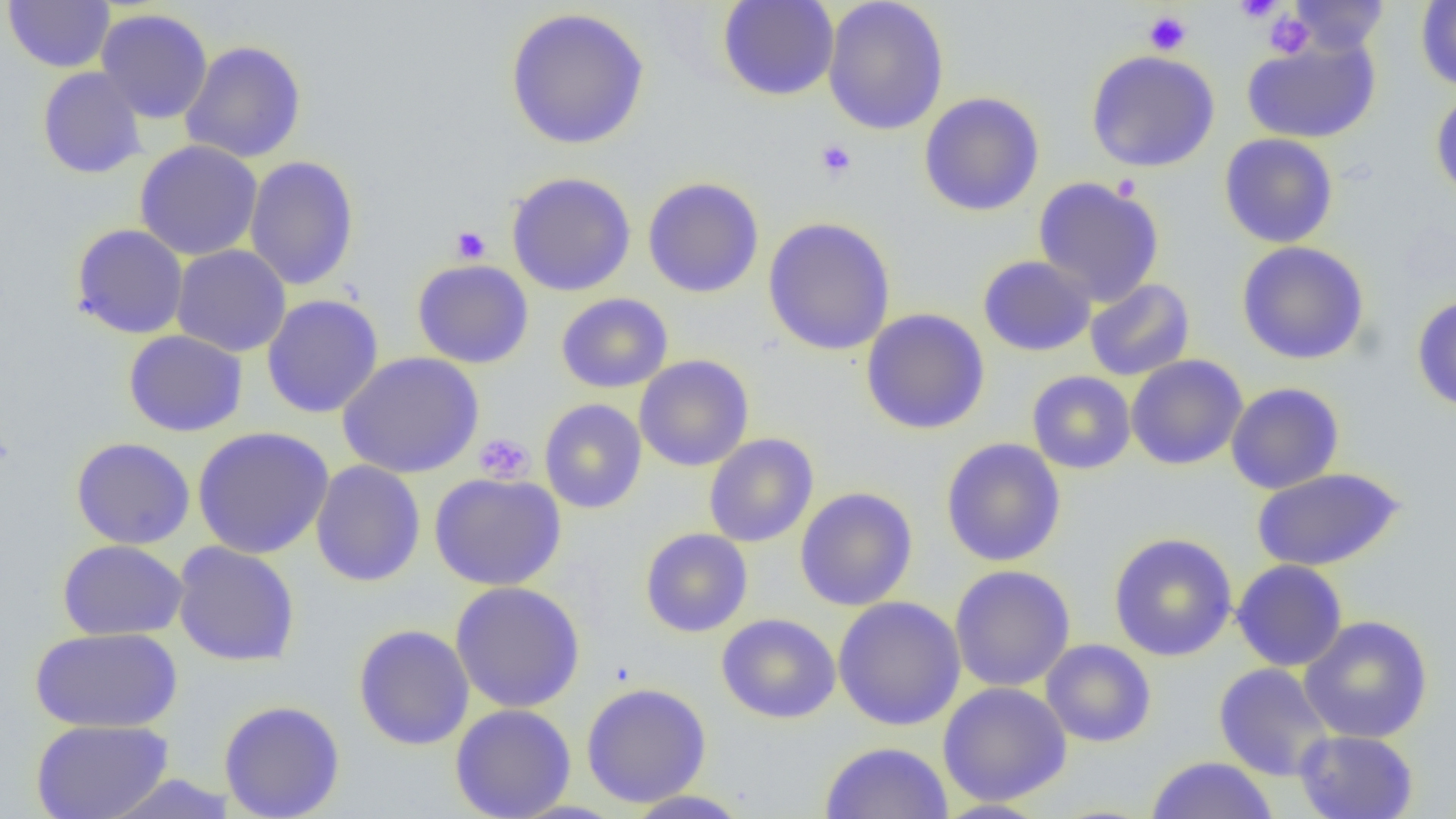

slide-level diagnosis = no evidence of blood parasites
image size = 1456×819 pixels
platelet locations = approximate bounding boxes as named x1/y1/x2/y2 corners in pixels: (x1=1234, y1=0, x2=1284, y2=23), (x1=1143, y1=11, x2=1192, y2=55), (x1=1264, y1=12, x2=1314, y2=59), (x1=815, y1=139, x2=857, y2=181), (x1=450, y1=226, x2=491, y2=264), (x1=474, y1=433, x2=536, y2=484)
magnification = 1000x
modality = optical microscopy
field of view = single
uninfected red blood cell locations = approximate bounding boxes as named x1/y1/x2/y2 corners in pixels: (x1=4, y1=0, x2=115, y2=73), (x1=717, y1=0, x2=840, y2=101), (x1=1288, y1=0, x2=1389, y2=54), (x1=822, y1=1, x2=950, y2=136), (x1=1416, y1=1, x2=1456, y2=91), (x1=505, y1=7, x2=650, y2=150), (x1=96, y1=8, x2=213, y2=124), (x1=1241, y1=36, x2=1380, y2=144), (x1=179, y1=40, x2=308, y2=163), (x1=1085, y1=49, x2=1220, y2=173), (x1=37, y1=67, x2=147, y2=179), (x1=1430, y1=89, x2=1456, y2=202), (x1=919, y1=91, x2=1045, y2=216), (x1=1218, y1=133, x2=1339, y2=248), (x1=134, y1=141, x2=263, y2=261), (x1=244, y1=155, x2=360, y2=290), (x1=507, y1=172, x2=636, y2=296), (x1=1033, y1=176, x2=1165, y2=307), (x1=642, y1=177, x2=765, y2=298), (x1=762, y1=216, x2=896, y2=356), (x1=71, y1=223, x2=188, y2=339), (x1=1236, y1=241, x2=1370, y2=365), (x1=171, y1=244, x2=291, y2=357), (x1=977, y1=255, x2=1096, y2=356), (x1=412, y1=259, x2=534, y2=369), (x1=1084, y1=278, x2=1195, y2=381), (x1=556, y1=292, x2=673, y2=393), (x1=261, y1=294, x2=384, y2=418), (x1=1411, y1=295, x2=1456, y2=413), (x1=860, y1=308, x2=990, y2=435), (x1=123, y1=330, x2=248, y2=437), (x1=337, y1=352, x2=484, y2=479), (x1=634, y1=355, x2=754, y2=472), (x1=1125, y1=355, x2=1248, y2=470), (x1=1026, y1=370, x2=1136, y2=474), (x1=1225, y1=382, x2=1345, y2=494), (x1=539, y1=398, x2=647, y2=514), (x1=192, y1=426, x2=334, y2=559), (x1=704, y1=432, x2=819, y2=547), (x1=70, y1=437, x2=195, y2=549), (x1=940, y1=438, x2=1066, y2=567), (x1=310, y1=460, x2=426, y2=587), (x1=1251, y1=467, x2=1405, y2=571), (x1=429, y1=472, x2=566, y2=591), (x1=794, y1=487, x2=918, y2=611), (x1=640, y1=528, x2=753, y2=637), (x1=1108, y1=532, x2=1238, y2=661), (x1=58, y1=539, x2=188, y2=641), (x1=172, y1=541, x2=300, y2=667), (x1=1231, y1=559, x2=1348, y2=672), (x1=950, y1=564, x2=1076, y2=692), (x1=450, y1=581, x2=585, y2=713), (x1=833, y1=596, x2=966, y2=731), (x1=716, y1=613, x2=841, y2=724), (x1=1299, y1=615, x2=1434, y2=744), (x1=353, y1=624, x2=475, y2=750), (x1=30, y1=626, x2=183, y2=733), (x1=1041, y1=639, x2=1157, y2=747), (x1=1213, y1=662, x2=1335, y2=781), (x1=580, y1=682, x2=712, y2=807), (x1=937, y1=682, x2=1072, y2=806), (x1=219, y1=700, x2=345, y2=819), (x1=450, y1=704, x2=576, y2=819), (x1=30, y1=719, x2=174, y2=819), (x1=1294, y1=729, x2=1419, y2=819), (x1=819, y1=740, x2=953, y2=819), (x1=1146, y1=756, x2=1279, y2=819), (x1=102, y1=773, x2=238, y2=818), (x1=623, y1=790, x2=754, y2=818), (x1=932, y1=799, x2=1051, y2=818)
preparation = thin blood smear